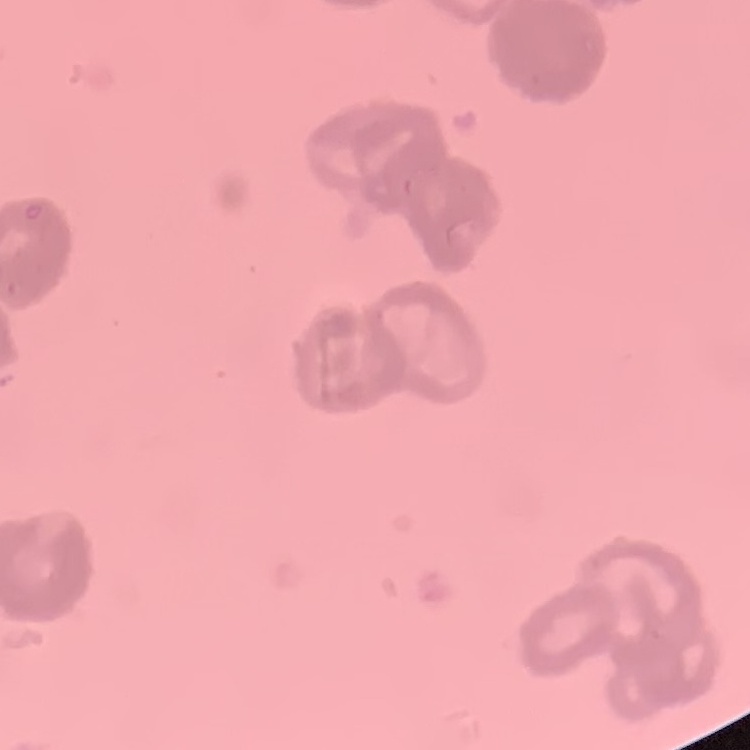
Summary:
  - Red blood cell morphology: rouleaux formation
  - Image type: square crop of a larger photomicrograph
  - Preparation: thin blood smear
  - Stain: Field's or Giemsa